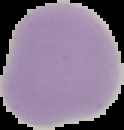

image_type: cell region segmented out of the field of view; surrounding area masked to black
image_size: 124×130 pixels
preparation: thin blood film
result: no malaria parasites seen